State which parasite is depicted.
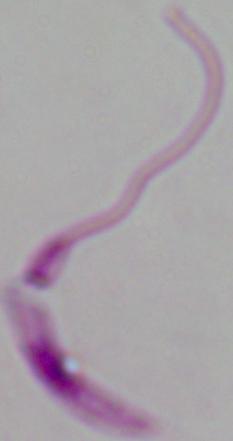

Leishmania.

{
  "modality": "micrograph",
  "magnification": "1000x"
}